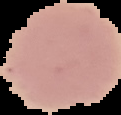
Malaria status: uninfected. Image is 121×115 pixels. Cell region segmented out of the field of view; the surrounding area is masked to black. From a thin blood smear.